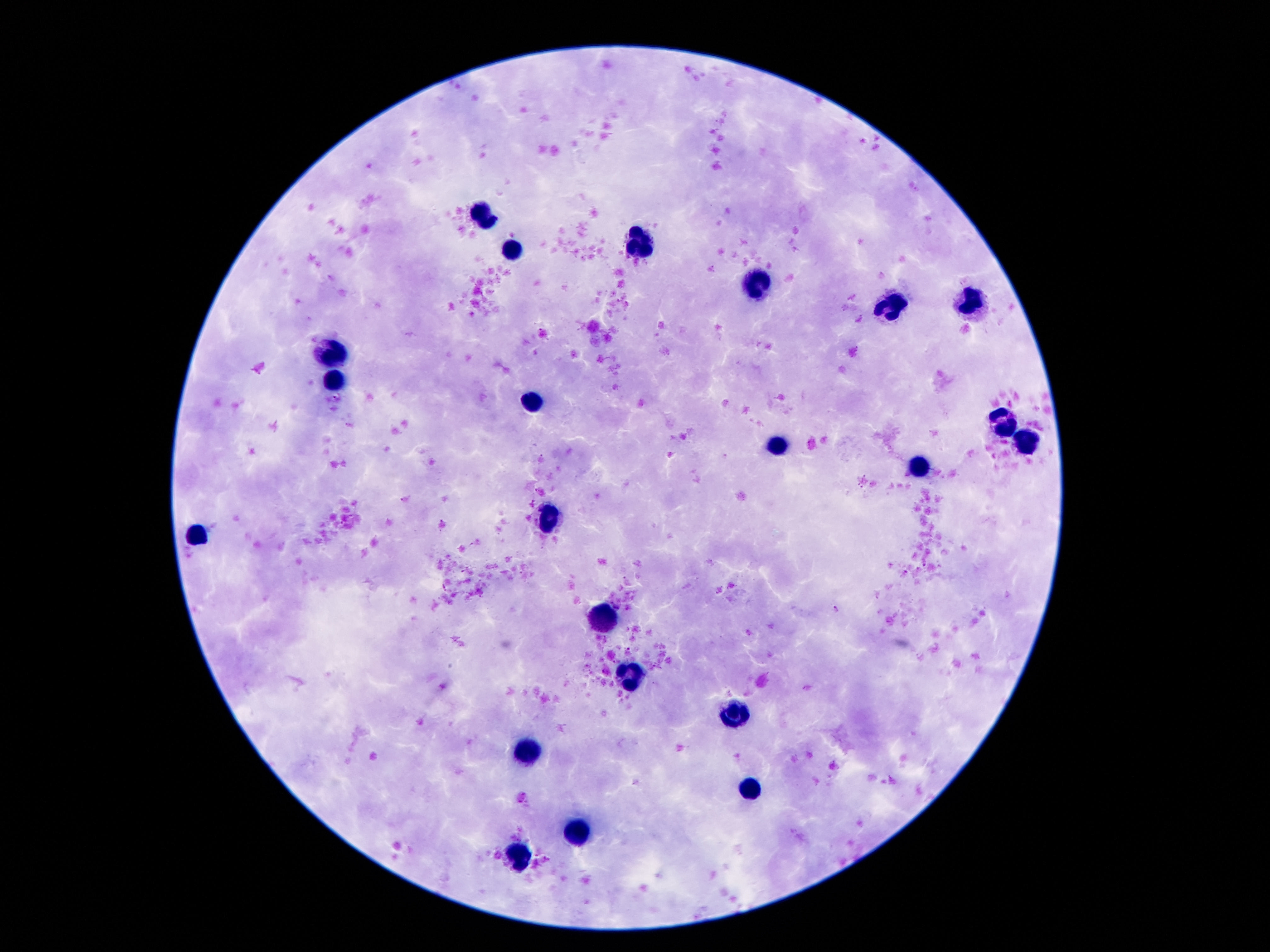
Approximate centers as {x, y} in pixels.
Summary:
  - Leukocyte locations: {487, 215}, {646, 241}, {513, 250}, {760, 281}, {970, 302}, {898, 306}, {333, 351}, {335, 378}, {531, 400}, {1005, 423}, {1026, 439}, {781, 446}, {921, 469}, {548, 515}, {195, 535}, {601, 618}, {629, 674}, {734, 714}, {529, 754}, {748, 784}, {580, 831}, {517, 852}
  - Preparation: thick peripheral-blood smear
  - Magnification: 100x
  - Patient malaria status: not infected
  - Image size: 1270×952 pixels
  - Field of view: single
  - Stain: Giemsa
  - Capture: smartphone camera through the microscope eyepiece